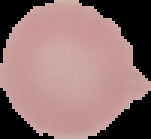
Image is 151×139 pixels. From a thin blood film. Segmented cell region on a black background. Result: no Plasmodium parasites seen.